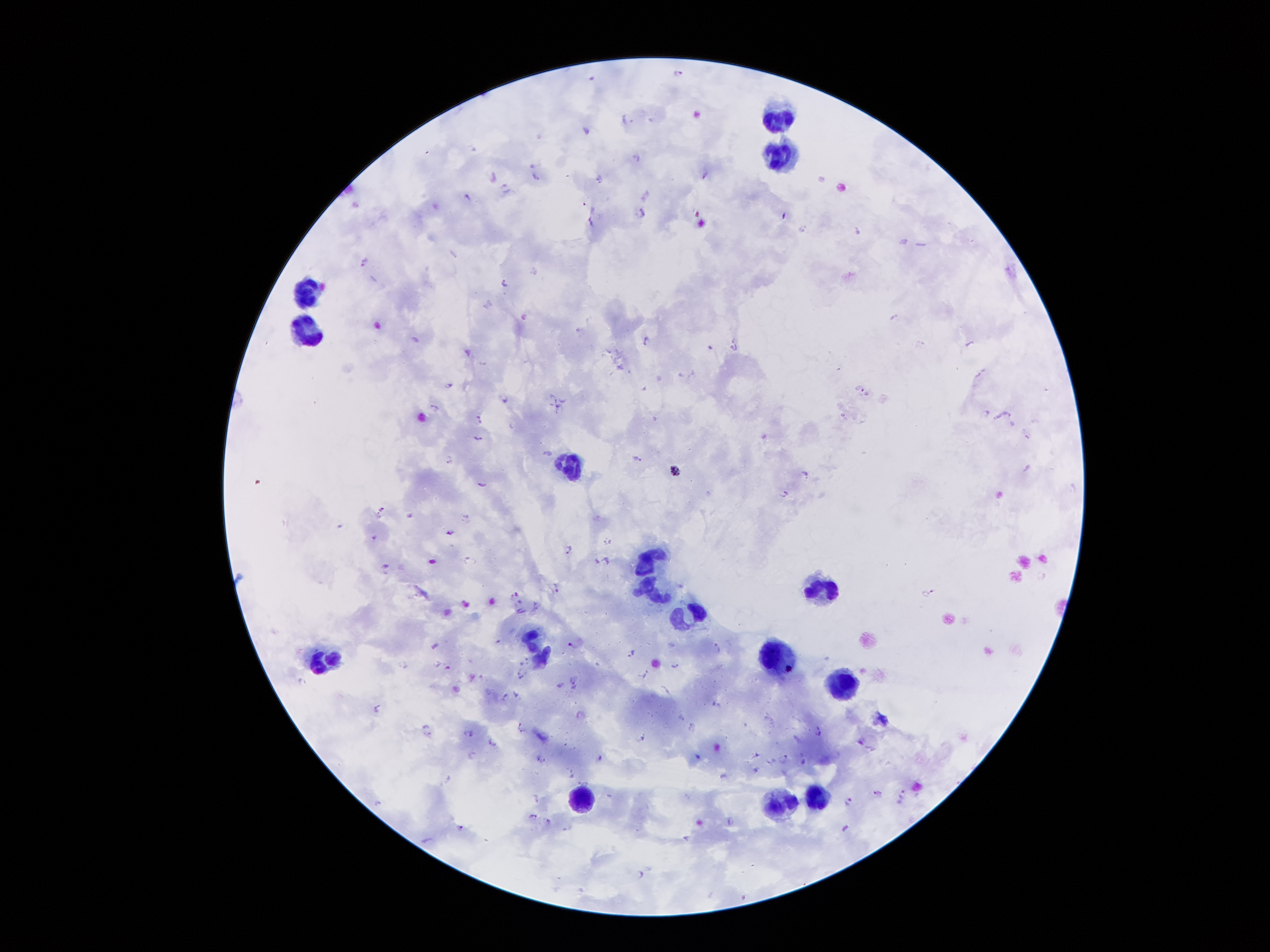

coordinate format = approximate centers as (x, y) in pixels
leukocyte locations = (772, 115), (781, 153), (308, 292), (304, 324), (573, 469), (649, 558), (822, 587), (651, 588), (694, 618), (533, 637), (776, 653), (542, 658), (323, 661), (848, 686), (818, 796), (581, 801), (781, 804)
malaria parasite locations = (630, 118), (585, 130), (634, 157), (704, 175), (536, 176), (507, 187), (465, 196), (641, 210), (784, 213), (590, 218), (802, 227), (856, 231), (363, 263), (504, 284), (896, 315), (646, 338), (467, 353), (484, 363), (448, 385), (860, 386), (503, 400), (562, 400), (436, 406), (556, 406), (986, 412), (1006, 412), (478, 419), (1025, 435), (764, 436), (479, 439), (449, 460), (639, 460), (1026, 468), (675, 469), (805, 472), (479, 484), (784, 492), (380, 509), (410, 514), (448, 529), (375, 537), (607, 541), (568, 550), (469, 559), (596, 560), (606, 560), (385, 566), (557, 588), (932, 591), (516, 594), (520, 601), (536, 606), (524, 611), (497, 642), (570, 643), (435, 646), (717, 648), (632, 653), (524, 661), (436, 664), (672, 665), (447, 667), (646, 670), (519, 674), (572, 681), (558, 684), (516, 694), (505, 695), (713, 705), (377, 707), (581, 713), (521, 727), (425, 729), (817, 731), (470, 733), (643, 739), (859, 741), (494, 742), (755, 754), (473, 756), (599, 756), (784, 757), (541, 759), (803, 762), (753, 768), (876, 794), (904, 794), (848, 802), (534, 815), (547, 820), (729, 822), (847, 827), (460, 828), (684, 837), (426, 841), (643, 872)
stain = Giemsa
image size = 1270×952 pixels
capture = smartphone camera through the microscope eyepiece
preparation = thick blood smear
magnification = 100x
patient malaria status = infected with Plasmodium falciparum
field of view = single